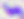

Summary:
  - Magnification: 400x
  - Modality: photomicrograph
  - Identification: Toxoplasma gondii